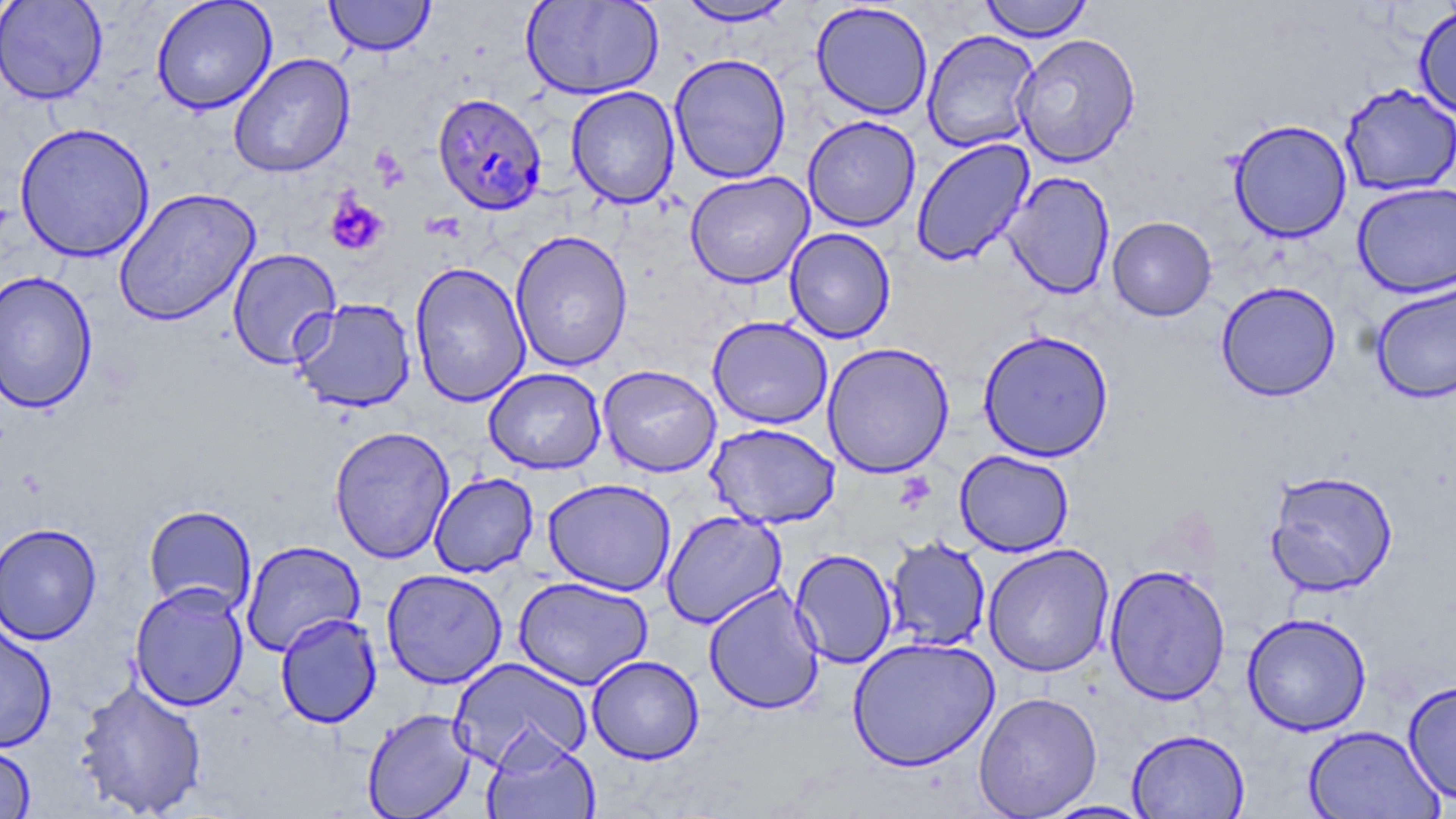
Approximate bounding boxes as [x1, y1, x2, y2] in pixels. Plasmodium falciparum-infected red blood cell locations: [432, 93, 548, 215]. Platelet locations: [325, 193, 389, 256]. Uninfected red blood cell locations: [0, 0, 108, 105], [151, 0, 277, 114], [324, 0, 435, 56], [521, 0, 665, 100], [979, 0, 1092, 42], [676, 1, 798, 27], [811, 2, 933, 120], [1413, 5, 1456, 120], [922, 29, 1040, 153], [1013, 32, 1142, 167], [228, 53, 355, 178], [669, 53, 792, 184], [1339, 83, 1456, 196], [566, 86, 680, 208], [802, 115, 921, 232], [1227, 119, 1352, 243], [14, 122, 155, 263], [911, 138, 1035, 267], [684, 171, 814, 288], [1003, 171, 1115, 299], [1352, 181, 1456, 298], [113, 187, 261, 327], [1107, 216, 1217, 321], [784, 227, 896, 343], [510, 230, 633, 372], [227, 248, 342, 370], [410, 262, 531, 407], [0, 269, 98, 413], [1216, 281, 1341, 401], [1371, 282, 1456, 404], [291, 298, 417, 413], [707, 316, 833, 429], [978, 328, 1115, 462], [822, 342, 955, 478], [598, 364, 721, 477], [483, 368, 606, 474], [705, 422, 841, 528], [329, 425, 455, 564], [954, 450, 1074, 556], [1265, 470, 1399, 596], [428, 472, 539, 578], [542, 478, 676, 596], [143, 504, 257, 616], [661, 509, 786, 628], [1, 522, 102, 645], [885, 536, 991, 652], [241, 540, 365, 656], [983, 543, 1114, 677], [790, 549, 898, 668], [1104, 564, 1231, 705], [381, 569, 508, 689], [513, 576, 653, 690], [129, 582, 249, 712], [703, 584, 824, 715], [275, 612, 382, 728], [1242, 613, 1372, 735], [0, 620, 57, 752], [846, 636, 1000, 771], [587, 655, 704, 764], [450, 657, 593, 774], [74, 677, 208, 818], [1402, 679, 1456, 805], [973, 691, 1103, 818], [362, 708, 477, 819], [1303, 724, 1445, 818], [1126, 728, 1250, 818], [482, 731, 601, 819], [0, 741, 37, 818], [1041, 800, 1156, 818]. Slide-level diagnosis: Plasmodium falciparum. Light microscopy. Single field of view. Thin blood film. Image is 1456×819 pixels. May-Grünwald-Giemsa-stained preparation. 1000x magnification.